Give the extent of all Plasmodium vivax-infected red blood cells.
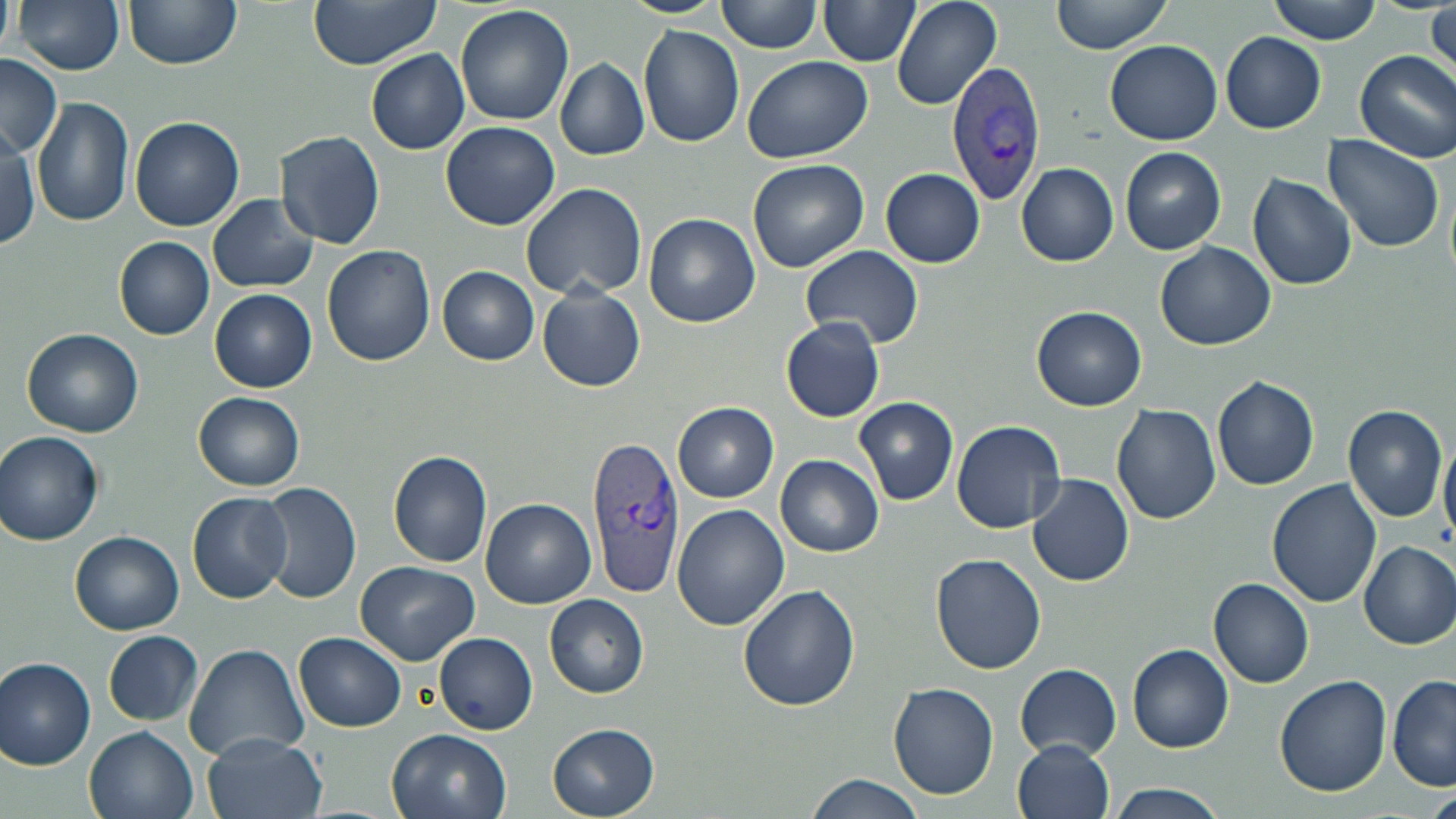

Approximate bounding boxes as (x1,y1)-(x2,y2) corner pairs in pixels.
Plasmodium vivax-infected red blood cells: (946,59)-(1048,204), (585,436)-(685,597).

Uninfected red blood cell locations: (0,0)-(16,52), (13,0)-(125,76), (123,0)-(241,70), (308,0)-(443,70), (623,0)-(726,18), (891,0)-(1002,111), (1050,0)-(1171,55), (1268,0)-(1383,43), (718,1)-(824,54), (817,1)-(920,66), (455,5)-(574,128), (1430,5)-(1456,82), (639,25)-(745,149), (1222,32)-(1327,132), (1104,40)-(1224,146), (367,49)-(469,154), (1353,50)-(1456,164), (1,54)-(63,157), (741,56)-(871,164), (556,59)-(649,160), (34,98)-(134,229), (130,116)-(243,232), (442,121)-(561,232), (276,131)-(385,249), (0,132)-(41,251), (1321,135)-(1446,252), (1120,147)-(1226,255), (748,159)-(868,273), (1017,163)-(1119,266), (881,168)-(985,268), (1248,173)-(1356,292), (520,180)-(647,300), (208,193)-(320,294), (645,214)-(759,327), (115,237)-(215,340), (1155,241)-(1276,350), (322,244)-(435,366), (799,245)-(923,348), (437,266)-(540,364), (537,283)-(645,393), (210,289)-(316,392), (1032,306)-(1147,412), (781,318)-(884,422), (23,328)-(143,438), (1211,375)-(1320,491), (194,392)-(305,490), (854,397)-(958,505), (674,402)-(779,503), (1112,403)-(1222,524), (1341,404)-(1448,523), (951,420)-(1066,534), (1,431)-(104,545), (1439,438)-(1456,538), (389,450)-(494,567), (776,455)-(884,557), (1028,473)-(1134,586), (1266,478)-(1381,608), (258,482)-(360,605), (187,493)-(295,604), (481,499)-(597,608), (674,504)-(788,631), (70,531)-(185,635), (1358,540)-(1456,650), (930,554)-(1046,675), (357,560)-(479,666), (1209,577)-(1314,688), (738,583)-(862,712), (544,594)-(649,698), (103,630)-(205,726), (295,633)-(406,731), (434,633)-(537,734), (183,641)-(311,762), (1127,645)-(1233,753), (0,656)-(98,769), (1016,663)-(1122,758), (1388,674)-(1456,791), (1275,675)-(1392,796), (889,682)-(999,800), (548,724)-(660,817), (85,725)-(198,819), (385,728)-(511,819), (201,734)-(326,819), (1012,739)-(1116,819), (802,778)-(925,819), (1106,782)-(1230,819), (1427,791)-(1456,819). Slide-level diagnosis: Plasmodium vivax. 1000x magnification. Thin blood film. Single field of view. May-Grünwald-Giemsa-stained preparation. Optical microscopy. Image is 1456×819 pixels.